Look for Plasmodium parasites.
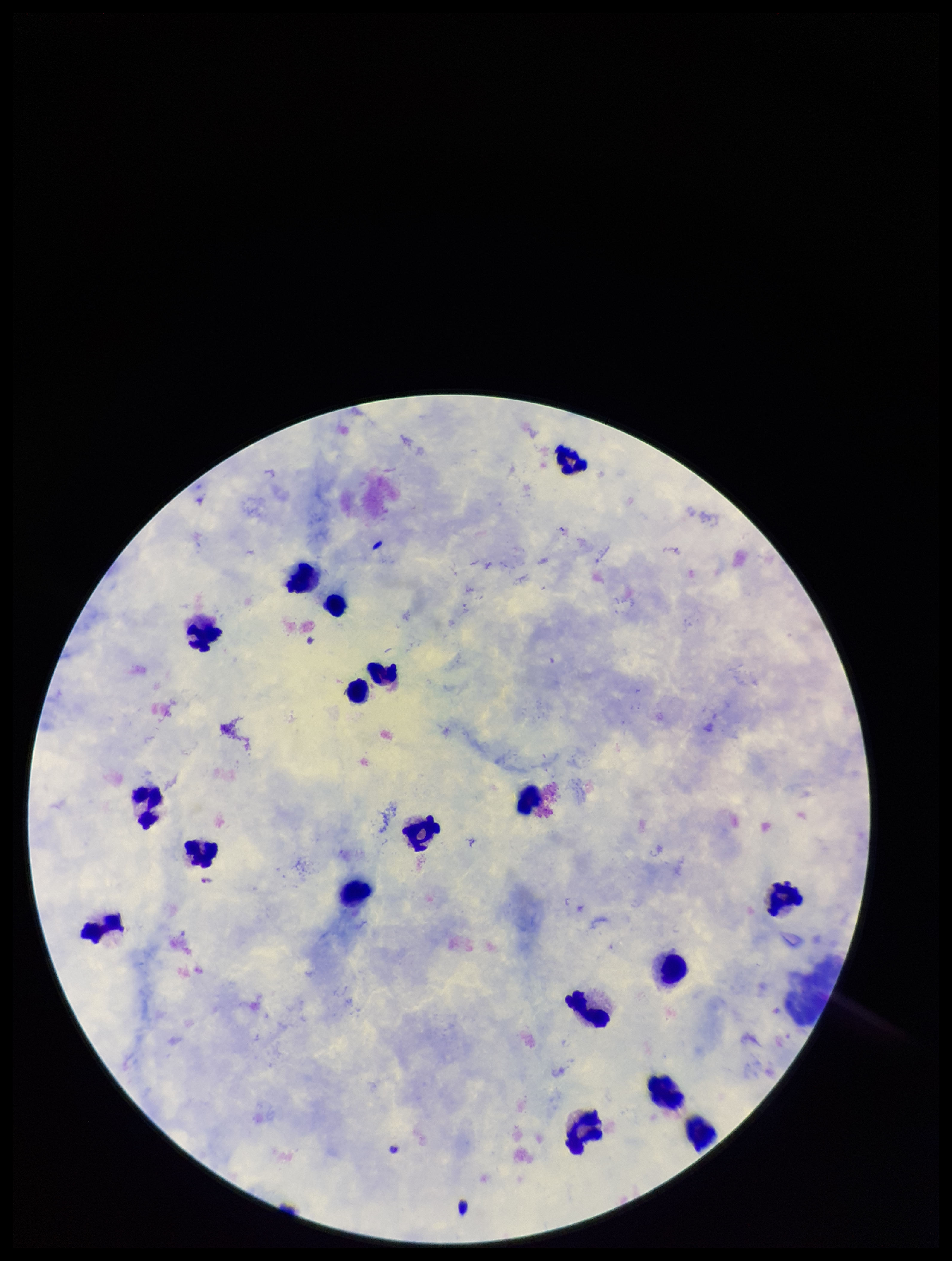
None identified.

field of view = one from this slide
patient malaria status = positive
capture = smartphone photograph through the microscope eyepiece
image size = 952×1261 pixels
stain = Giemsa
leukocyte count = 18
preparation = thick smear
species reported for this patient = Plasmodium falciparum
parasite count = 0